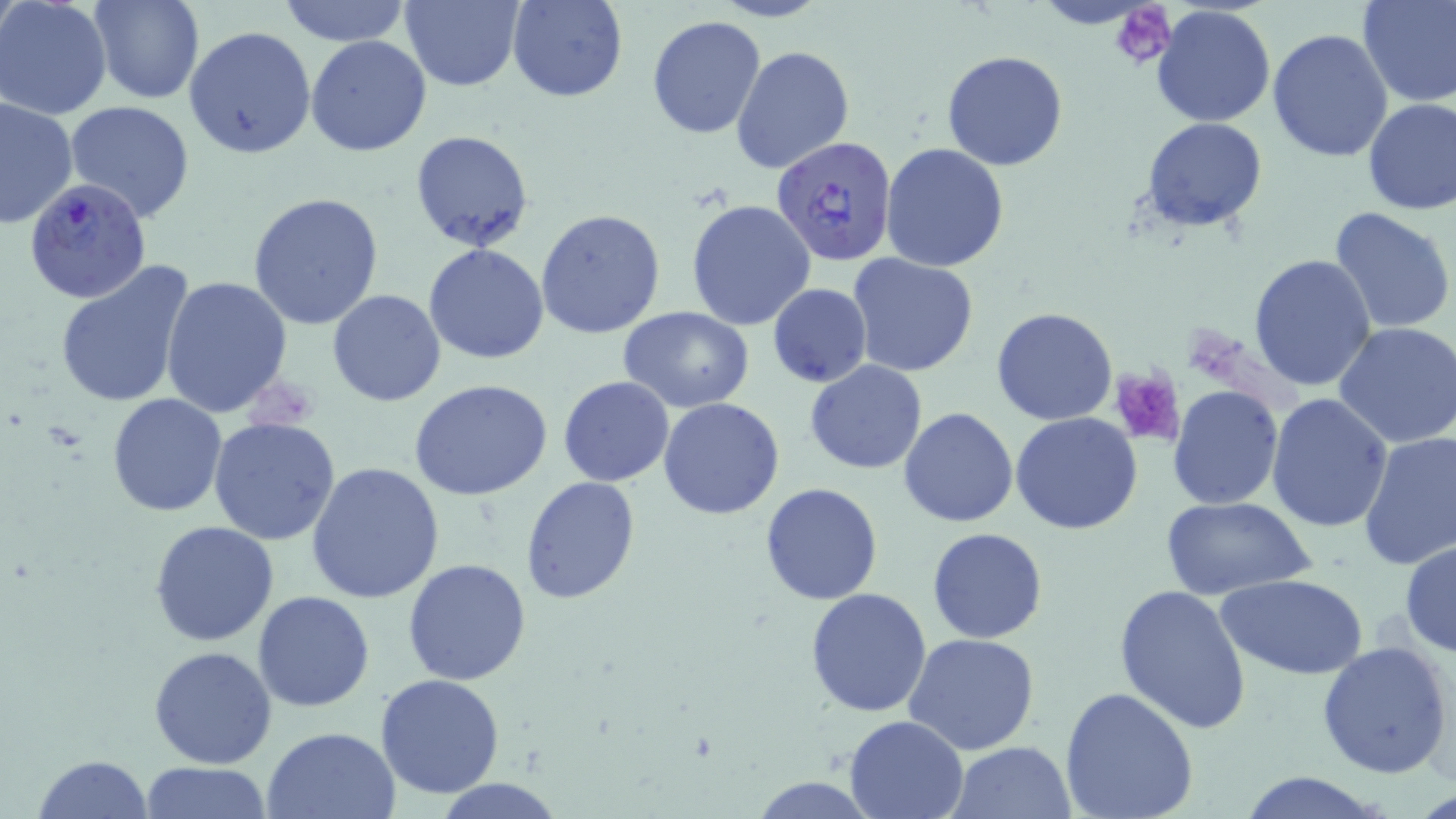
Summary:
  - Coordinate format: approximate bounding boxes as [x1, y1, x2, y2] in pixels
  - Platelet locations: [1110, 3, 1175, 69], [1112, 368, 1186, 445]
  - Uninfected red blood cell locations: [0, 0, 112, 120], [91, 0, 203, 104], [278, 0, 411, 47], [401, 0, 524, 91], [508, 0, 628, 102], [712, 0, 827, 23], [1031, 0, 1159, 28], [1358, 0, 1456, 106], [1152, 5, 1278, 128], [646, 16, 767, 138], [183, 26, 317, 160], [1268, 27, 1395, 163], [306, 35, 432, 158], [731, 45, 854, 174], [942, 49, 1069, 171], [0, 98, 78, 230], [1363, 99, 1456, 217], [65, 100, 197, 224], [1142, 117, 1267, 232], [410, 129, 534, 250], [880, 143, 1010, 271], [247, 190, 383, 330], [685, 199, 816, 330], [1328, 205, 1455, 334], [536, 208, 666, 340], [423, 244, 550, 365], [847, 252, 981, 379], [1249, 254, 1379, 393], [54, 259, 197, 409], [161, 275, 294, 416], [768, 284, 872, 387], [781, 284, 896, 462], [326, 289, 448, 407], [618, 306, 754, 413], [990, 308, 1118, 426], [1334, 320, 1456, 450], [805, 360, 927, 475], [558, 376, 674, 487], [408, 380, 555, 501], [1168, 385, 1282, 509], [107, 392, 229, 516], [1266, 394, 1394, 533], [659, 398, 785, 519], [898, 408, 1019, 528], [1012, 411, 1143, 534], [207, 416, 341, 544], [1357, 431, 1456, 570], [306, 460, 445, 603], [520, 476, 640, 605], [760, 482, 884, 605], [1161, 495, 1317, 602], [149, 521, 279, 648], [927, 527, 1049, 644], [1400, 540, 1456, 657], [402, 558, 530, 686], [1216, 574, 1368, 679], [1114, 584, 1252, 734], [804, 588, 934, 718], [253, 591, 376, 711], [904, 633, 1041, 754], [1317, 640, 1454, 779], [148, 645, 277, 769], [375, 672, 505, 799], [1059, 686, 1200, 819], [842, 715, 968, 819], [261, 726, 401, 819], [949, 741, 1075, 818], [32, 753, 153, 819], [137, 761, 273, 817], [1234, 772, 1393, 818], [747, 776, 882, 816], [433, 779, 566, 818]
  - Plasmodium falciparum-infected red blood cell locations: [770, 136, 900, 267], [24, 178, 151, 304]
  - Slide-level diagnosis: Plasmodium falciparum
  - Modality: optical microscopy
  - Field of view: single
  - Magnification: 1000x
  - Image size: 1456×819 pixels
  - Preparation: thin blood film
  - Stain: May-Grünwald-Giemsa